Name the parasite shown.
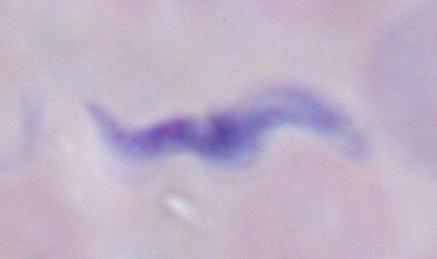
A trypanosome.

{
  "magnification": "1000x",
  "modality": "photomicrograph"
}